Locate every blood parasite and identify its species.
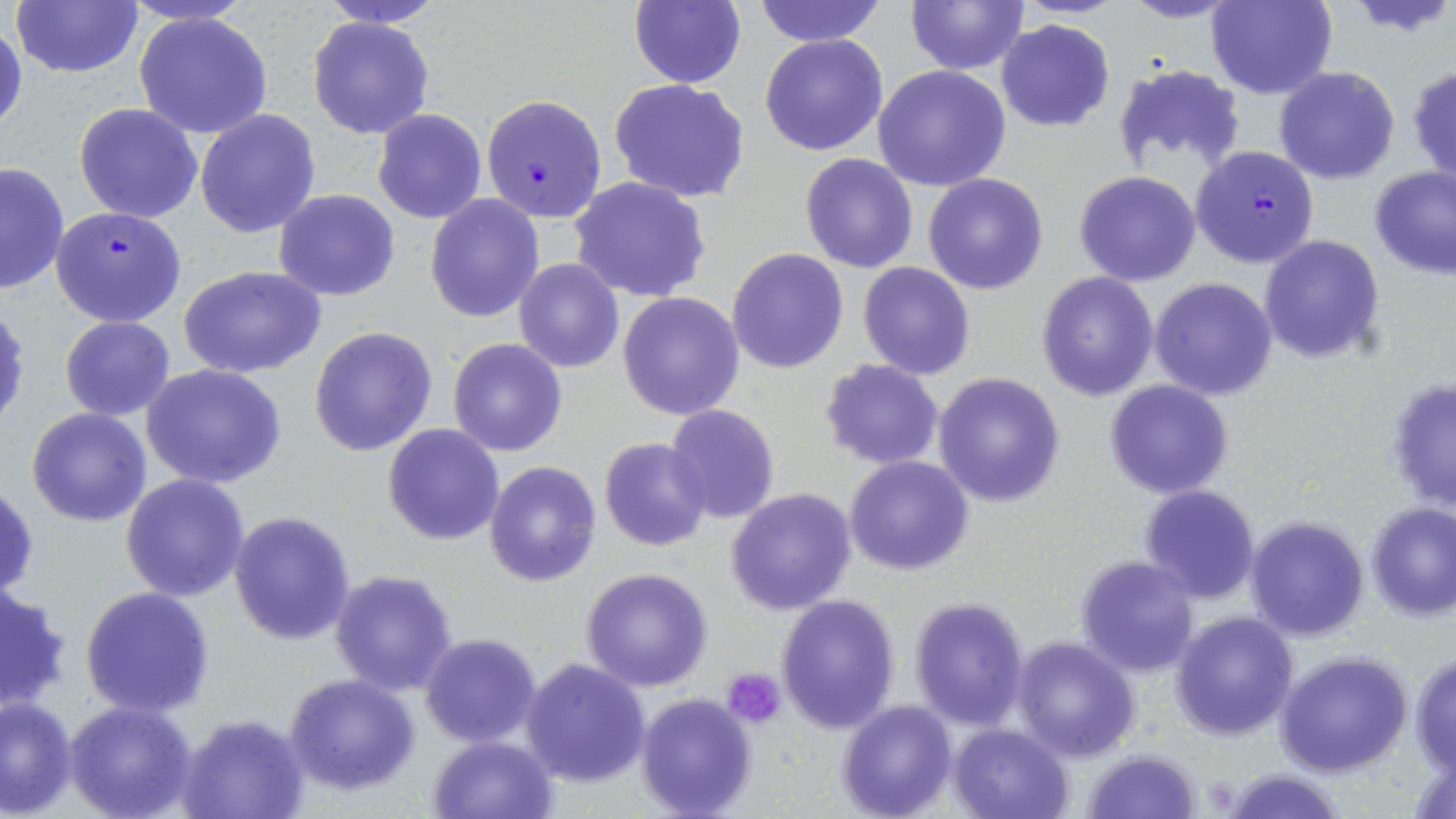

Approximate bounding boxes as named x1/y1/x2/y2 corners in pixels.
Plasmodium falciparum-infected red blood cells: (x1=481, y1=95, x2=606, y2=223), (x1=1192, y1=146, x2=1319, y2=269), (x1=50, y1=206, x2=185, y2=327).
No Plasmodium ovale, Plasmodium malariae, Plasmodium vivax, Babesia divergens, or Trypanosoma brucei observed.

Summary:
  - Uninfected red blood cell locations: (x1=10, y1=0, x2=145, y2=79), (x1=316, y1=0, x2=446, y2=28), (x1=628, y1=0, x2=747, y2=90), (x1=752, y1=0, x2=889, y2=47), (x1=905, y1=0, x2=1029, y2=74), (x1=1119, y1=0, x2=1242, y2=23), (x1=1206, y1=0, x2=1336, y2=99), (x1=1345, y1=0, x2=1456, y2=38), (x1=133, y1=12, x2=274, y2=140), (x1=307, y1=15, x2=434, y2=140), (x1=996, y1=20, x2=1114, y2=133), (x1=0, y1=21, x2=27, y2=142), (x1=759, y1=33, x2=890, y2=158), (x1=1111, y1=64, x2=1247, y2=175), (x1=1408, y1=64, x2=1456, y2=187), (x1=872, y1=65, x2=1012, y2=192), (x1=1273, y1=66, x2=1402, y2=185), (x1=609, y1=79, x2=751, y2=203), (x1=74, y1=102, x2=204, y2=223), (x1=195, y1=109, x2=322, y2=237), (x1=374, y1=109, x2=487, y2=223), (x1=800, y1=153, x2=918, y2=274), (x1=0, y1=160, x2=71, y2=295), (x1=1368, y1=166, x2=1456, y2=279), (x1=1074, y1=171, x2=1202, y2=287), (x1=923, y1=173, x2=1050, y2=295), (x1=569, y1=175, x2=711, y2=303), (x1=272, y1=189, x2=401, y2=301), (x1=425, y1=195, x2=543, y2=323), (x1=1259, y1=234, x2=1386, y2=366), (x1=726, y1=248, x2=850, y2=374), (x1=513, y1=258, x2=625, y2=373), (x1=857, y1=262, x2=976, y2=381), (x1=178, y1=264, x2=328, y2=379), (x1=1035, y1=272, x2=1160, y2=401), (x1=1149, y1=277, x2=1279, y2=402), (x1=617, y1=291, x2=745, y2=421), (x1=60, y1=316, x2=175, y2=420), (x1=309, y1=325, x2=438, y2=456), (x1=447, y1=337, x2=568, y2=457), (x1=819, y1=359, x2=946, y2=470), (x1=141, y1=364, x2=287, y2=489), (x1=933, y1=371, x2=1066, y2=506), (x1=1384, y1=377, x2=1455, y2=518), (x1=1103, y1=380, x2=1235, y2=500), (x1=664, y1=404, x2=780, y2=522), (x1=27, y1=408, x2=152, y2=527), (x1=382, y1=424, x2=506, y2=547), (x1=599, y1=438, x2=712, y2=552), (x1=843, y1=455, x2=973, y2=576), (x1=483, y1=460, x2=601, y2=587), (x1=121, y1=474, x2=250, y2=602), (x1=1, y1=480, x2=39, y2=605), (x1=1137, y1=485, x2=1261, y2=605), (x1=725, y1=487, x2=857, y2=615), (x1=1366, y1=503, x2=1456, y2=621), (x1=229, y1=511, x2=356, y2=647), (x1=1244, y1=515, x2=1370, y2=642), (x1=1075, y1=554, x2=1200, y2=677), (x1=580, y1=567, x2=713, y2=692), (x1=329, y1=569, x2=459, y2=697), (x1=0, y1=581, x2=74, y2=715), (x1=80, y1=585, x2=215, y2=718), (x1=775, y1=595, x2=901, y2=735), (x1=909, y1=597, x2=1031, y2=730), (x1=1170, y1=610, x2=1297, y2=740), (x1=420, y1=634, x2=543, y2=747), (x1=1011, y1=635, x2=1141, y2=761), (x1=1276, y1=651, x2=1412, y2=777), (x1=1409, y1=651, x2=1456, y2=772), (x1=520, y1=658, x2=651, y2=788), (x1=282, y1=673, x2=421, y2=793), (x1=635, y1=690, x2=759, y2=819), (x1=0, y1=695, x2=77, y2=816), (x1=66, y1=700, x2=199, y2=818), (x1=837, y1=700, x2=957, y2=819), (x1=178, y1=714, x2=310, y2=819), (x1=948, y1=723, x2=1073, y2=818), (x1=427, y1=735, x2=557, y2=817), (x1=1407, y1=739, x2=1456, y2=819), (x1=1081, y1=749, x2=1202, y2=819), (x1=1220, y1=769, x2=1348, y2=819)
  - Platelet locations: (x1=724, y1=668, x2=787, y2=728)
  - Slide-level diagnosis: Plasmodium falciparum
  - Stain: May-Grünwald-Giemsa
  - Image size: 1456×819 pixels
  - Preparation: thin blood smear
  - Magnification: 1000x
  - Modality: optical microscopy
  - Field of view: single